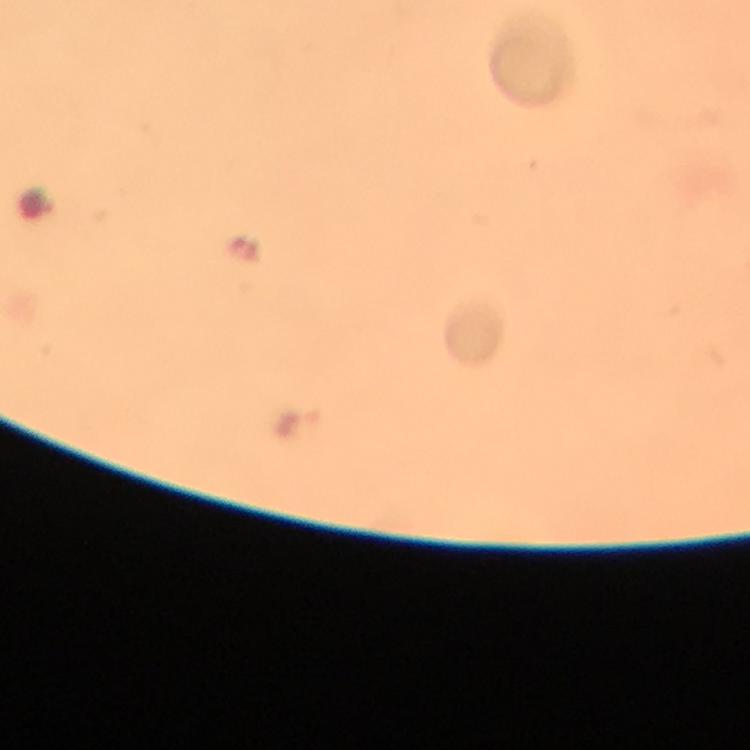
preparation = thick blood smear
malaria parasite locations = approximate object centers, in pixels from the top-left corner: (x=296, y=422)
cropped from = a single field of view
magnification = 100x
capture = smartphone photograph through a microscope
image size = 750×750 pixels
context = from a diagnostic examination for malaria
stain = Giemsa
immersion oil = used